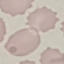
{
  "result": "no malaria parasites detected",
  "capture": "smartphone through the microscope eyepiece",
  "stain": "Giemsa",
  "image_type": "automatically extracted cell patch, resized to 64 × 64 pixels",
  "preparation": "thin blood smear"
}